Point out each leukocyte.
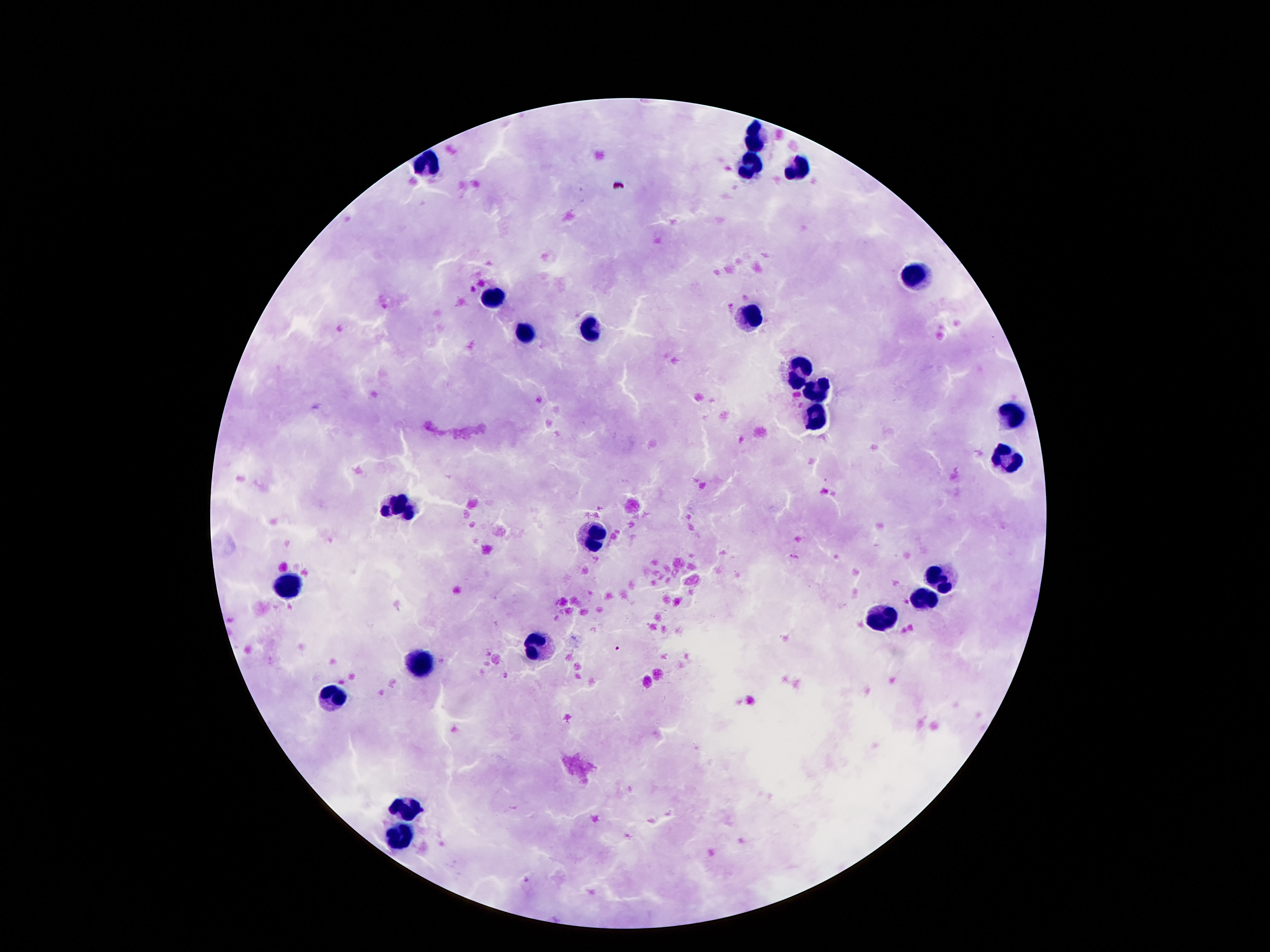
Approximate centers as {x, y} in pixels.
Leukocytes: {754, 136}, {429, 164}, {749, 168}, {800, 168}, {915, 276}, {493, 297}, {745, 314}, {592, 327}, {524, 333}, {800, 367}, {816, 394}, {1010, 414}, {818, 418}, {1003, 458}, {400, 504}, {593, 538}, {942, 580}, {289, 581}, {926, 599}, {886, 617}, {537, 644}, {420, 659}, {336, 694}, {407, 805}, {396, 836}.

image size = 1270×952 pixels
magnification = 100x
field of view = one from this slide
preparation = thick peripheral-blood smear
patient malaria status = negative
capture = smartphone camera through the microscope eyepiece
stain = Giemsa